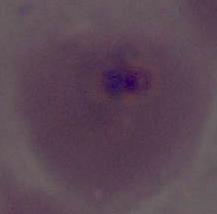

magnification = 400x or 1000x
modality = micrograph
identification = Plasmodium